Give the position of every Plasmodium parasite visible.
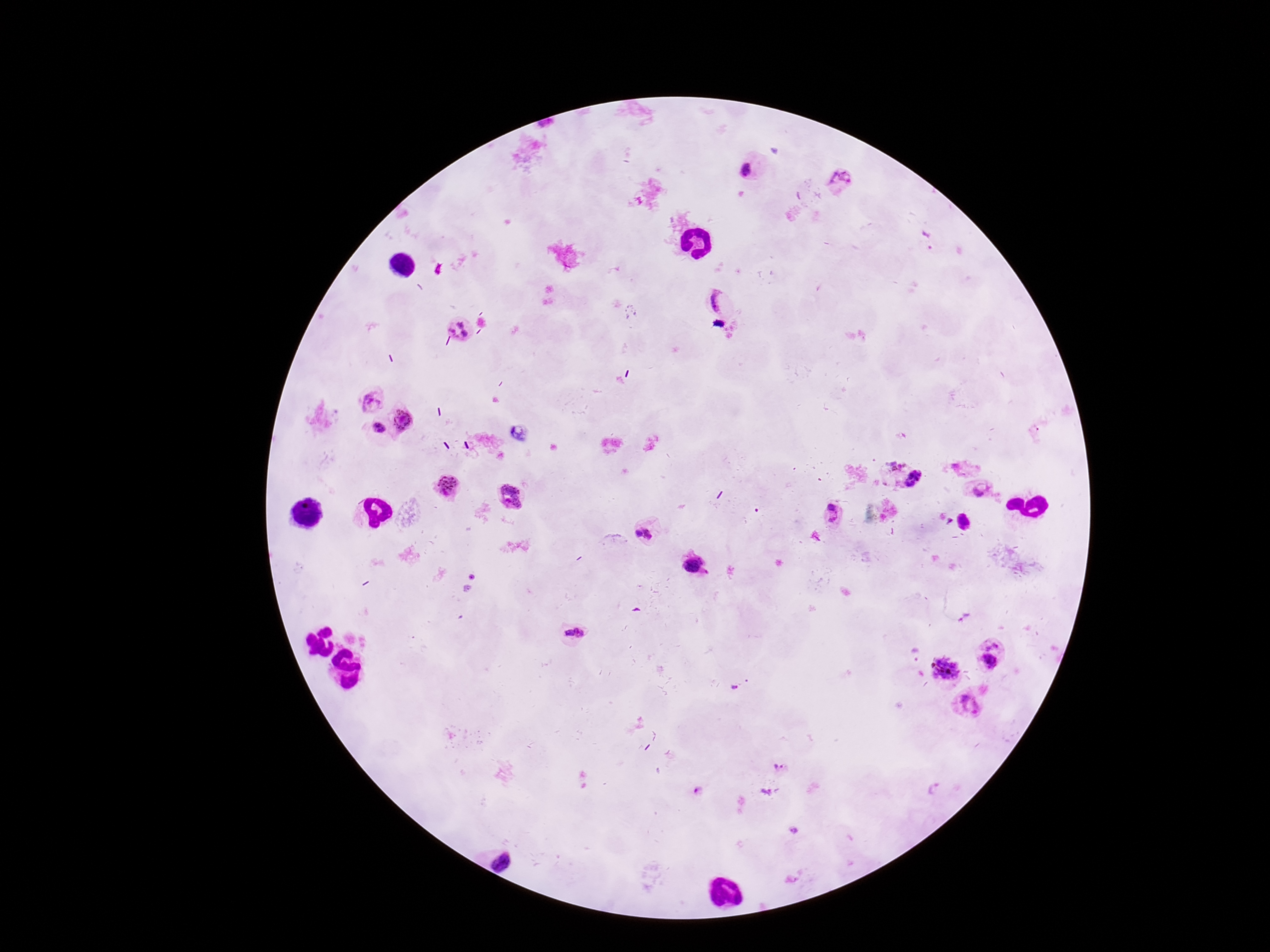
Approximate object centers, in pixels from the top-left corner.
Plasmodium parasites: (x=754, y=167), (x=841, y=180), (x=926, y=240), (x=716, y=301), (x=461, y=329), (x=372, y=400), (x=402, y=421), (x=376, y=427), (x=893, y=466), (x=917, y=481), (x=445, y=488), (x=980, y=489), (x=512, y=497), (x=833, y=514), (x=645, y=533), (x=694, y=564), (x=571, y=635), (x=996, y=654), (x=943, y=669), (x=735, y=688), (x=970, y=707), (x=780, y=768), (x=937, y=791), (x=698, y=792), (x=765, y=792), (x=794, y=830).

stain = Giemsa
magnification = 100x
capture = smartphone camera through the microscope eyepiece
preparation = thick blood smear
field of view = one from this slide
patient malaria status = infected
image size = 1270×952 pixels